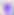

Toxoplasma gondii is seen. Photomicrograph. 400x magnification.